Report the malaria status of this cell.
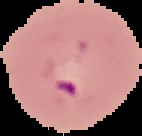
Parasitized.

From a thin blood film. Image is 142×136 pixels. Segmented cell region on a black background.